Report the malaria status of this cell.
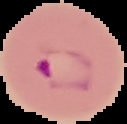
Parasitized.

preparation = thin blood smear
image type = cell region segmented out of the field of view; surrounding area masked to black
image size = 127×124 pixels